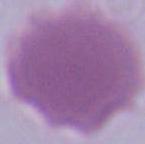
1000x magnification. Micrograph. A red blood cell is seen.